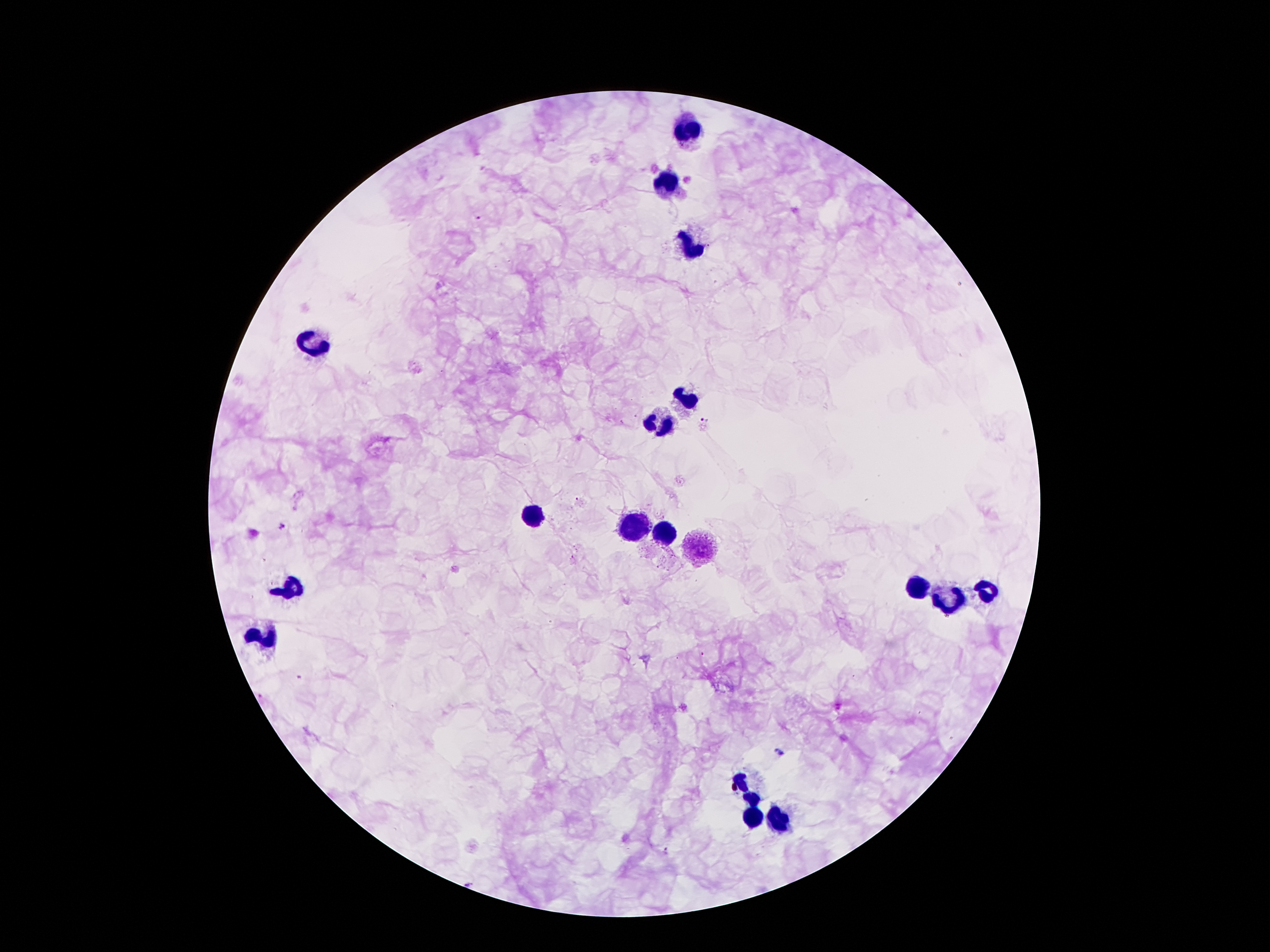

Approximate centers as [x, y] in pixels. Leukocyte locations: [683, 131], [671, 183], [691, 241], [313, 339], [685, 397], [661, 419], [533, 515], [633, 527], [663, 533], [701, 549], [921, 581], [287, 583], [983, 589], [951, 603], [263, 637], [749, 787], [751, 817], [777, 821]. Malaria parasite locations: [478, 217], [703, 422], [281, 526], [779, 751], [668, 849]. Image is 1270×952 pixels. 100x magnification. Patient malaria status: infected with Plasmodium falciparum. Photographed through the microscope eyepiece with a smartphone camera. Giemsa stain. Thick blood film. One field from this slide.